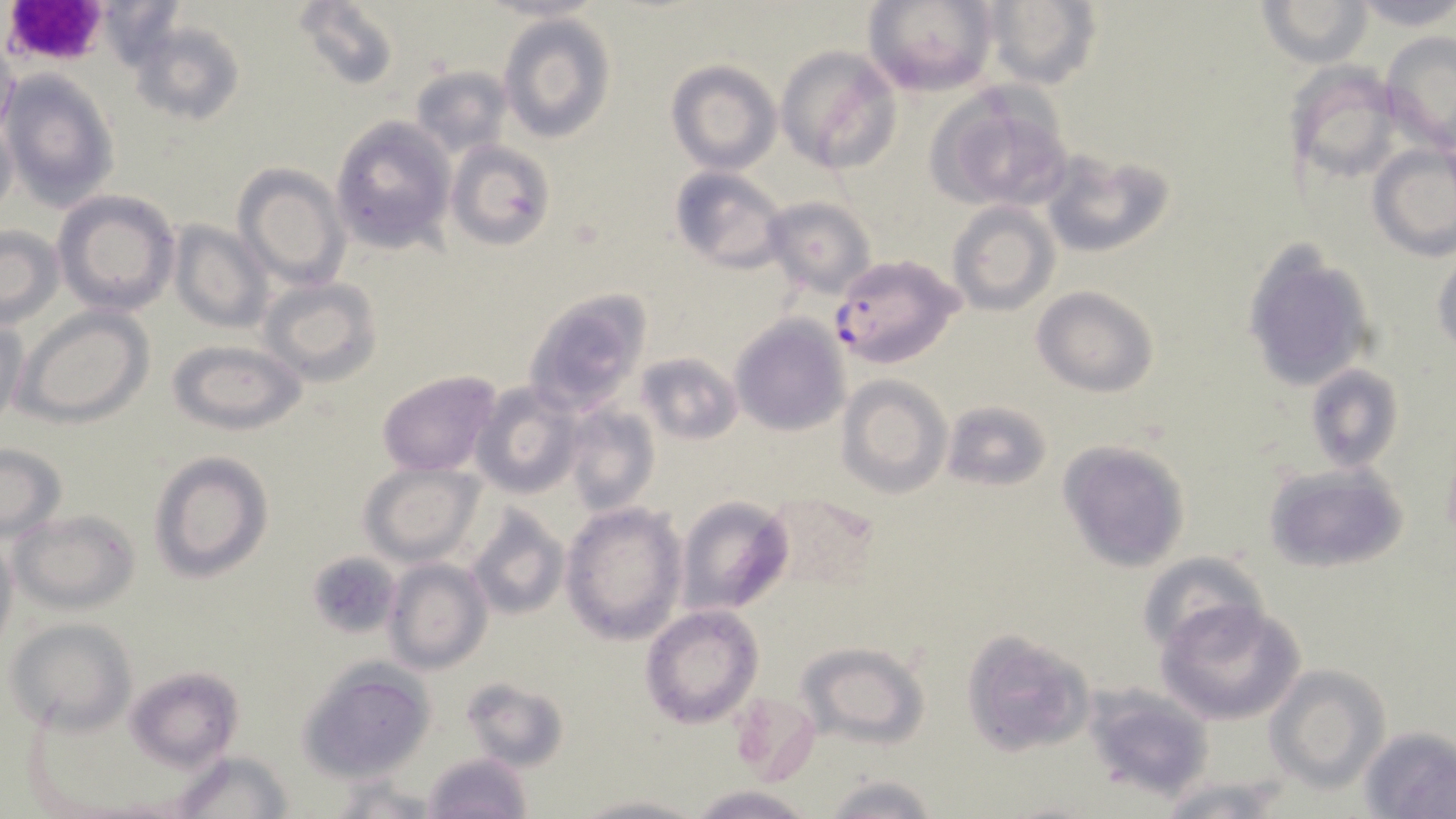 Approximate bounding boxes as (x1,y1)-(x2,y2) corner pairs in pixels. Plasmodium falciparum-infected red blood cell locations: (829,253)-(962,368). Platelet locations: (0,0)-(102,65). Uninfected red blood cell locations: (96,0)-(187,73), (292,0)-(401,92), (862,0)-(998,95), (979,0)-(1101,88), (1257,0)-(1375,66), (1349,0)-(1456,31), (498,14)-(615,143), (131,17)-(245,126), (1382,33)-(1456,154), (0,38)-(17,150), (777,45)-(902,173), (665,59)-(780,175), (1286,62)-(1400,184), (413,66)-(512,155), (3,69)-(121,209), (927,86)-(1074,211), (0,112)-(18,222), (329,116)-(454,252), (445,140)-(556,251), (1368,144)-(1456,259), (1041,150)-(1173,260), (232,163)-(352,289), (669,166)-(789,274), (54,190)-(181,316), (762,196)-(876,298), (947,201)-(1060,316), (166,219)-(274,333), (0,224)-(64,329), (1241,245)-(1377,393), (1431,254)-(1455,354), (259,277)-(383,387), (1033,285)-(1159,398), (523,288)-(652,417), (13,305)-(154,428), (729,315)-(850,436), (0,318)-(28,432), (168,338)-(305,436), (634,351)-(740,445), (1304,363)-(1405,475), (374,369)-(503,477), (838,374)-(952,499), (471,380)-(582,498), (943,399)-(1051,491), (561,404)-(659,517), (1056,440)-(1190,574), (0,442)-(66,541), (1440,442)-(1456,547), (148,449)-(275,582), (359,462)-(484,566), (1263,462)-(1410,575), (768,492)-(877,589), (676,496)-(794,615), (560,501)-(688,646), (466,505)-(569,621), (10,508)-(141,615), (0,532)-(18,651), (310,543)-(391,626), (1134,551)-(1269,657), (385,557)-(492,675), (1159,600)-(1304,725), (640,605)-(764,728), (6,617)-(138,733), (961,630)-(1095,757), (796,641)-(929,748), (298,659)-(436,779), (1266,664)-(1389,791), (125,666)-(243,769), (461,677)-(570,771), (1093,690)-(1211,794), (729,694)-(820,782), (1357,726)-(1456,819), (172,750)-(294,819), (421,751)-(534,819), (820,774)-(947,819), (328,777)-(445,817), (1157,780)-(1286,819), (685,785)-(814,818), (572,793)-(704,819). Slide-level diagnosis: Plasmodium falciparum. May-Grünwald-Giemsa stain. Optical microscopy. One field of a larger specimen. Thin blood smear. 1000x magnification. Image is 1456×819 pixels.